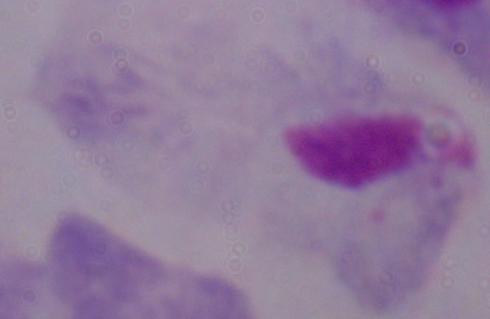
A trichomonad is shown. Photomicrograph. 1000x magnification.